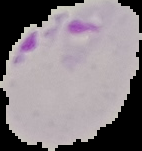 Result: malaria parasites detected. Image is 142×151 pixels. From a thin blood smear. The area outside the segmented cell region is set to black.